Report the malaria status of this cell.
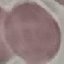

Uninfected.

Summary:
  - Stain: Giemsa
  - Capture: smartphone camera at the microscope eyepiece
  - Image type: cell patch, automatically extracted from a larger field of view and resized to 64 × 64 pixels
  - Preparation: thin smear